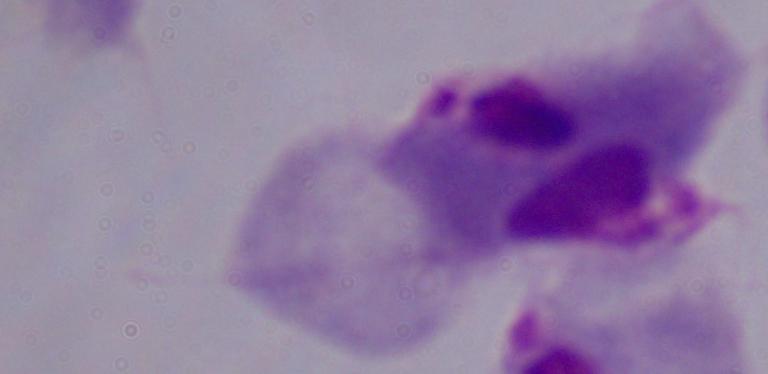
identification: trichomonad
modality: photomicrograph
magnification: 1000x